Name the cell type shown.
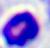
A leukocyte.

Summary:
  - Magnification: 400x
  - Modality: micrograph